Assess this cell for malaria.
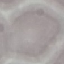
Uninfected.

Cell patch, automatically extracted from a larger field of view and resized to 64 × 64 pixels. Thin blood smear. Photographed with a smartphone camera at the microscope eyepiece. Giemsa stain.